Identify the blood parasite species.
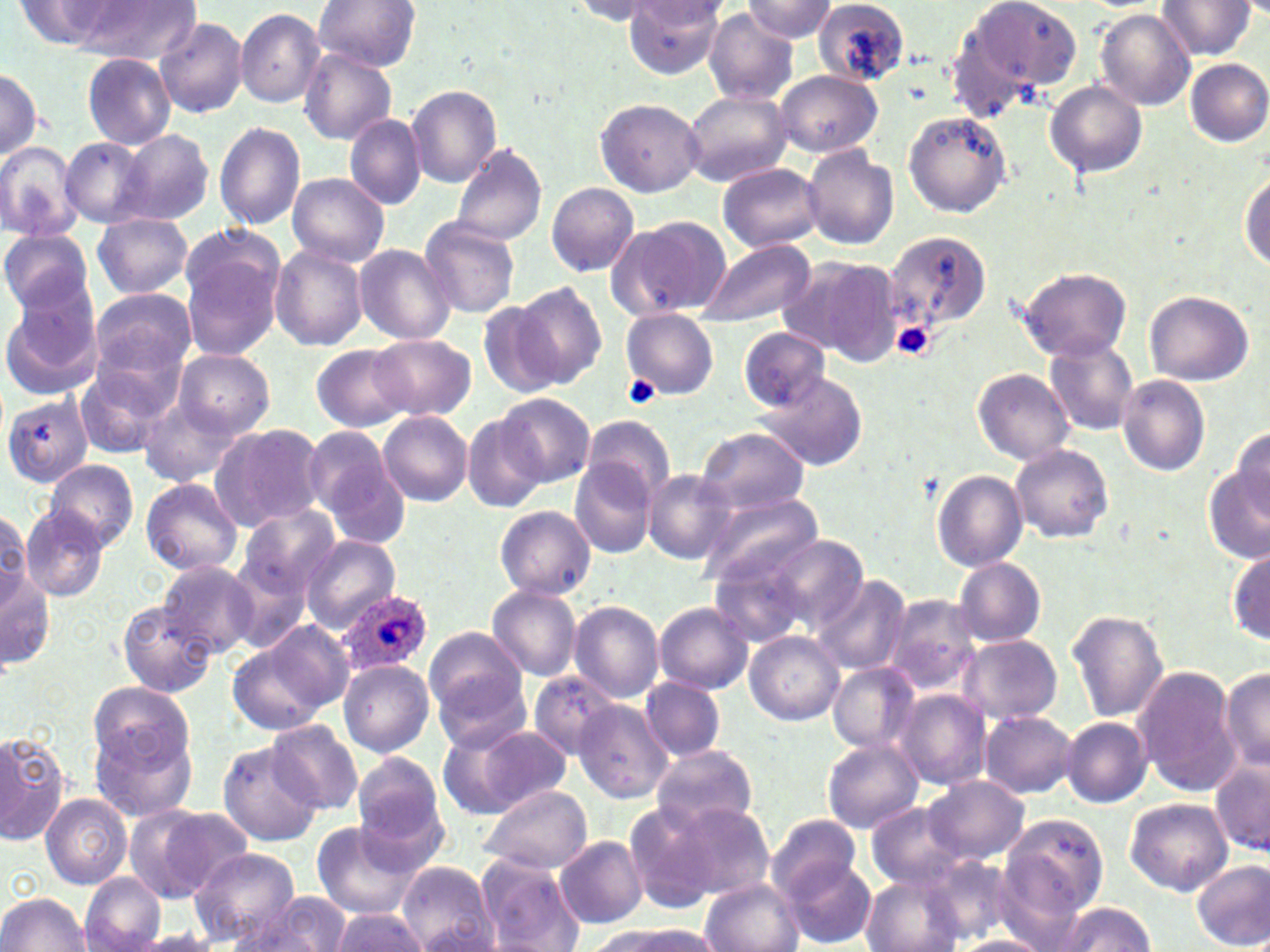
Plasmodium ovale.

Approximate bounding boxes as [x1, y1, x2, y2] in pixels. Platelet locations: [893, 321, 936, 361], [623, 374, 661, 409]. Uninfected red blood cell locations: [314, 0, 422, 72], [624, 0, 726, 78], [745, 0, 837, 42], [953, 0, 1082, 109], [813, 1, 910, 86], [1157, 1, 1258, 59], [12, 2, 143, 51], [61, 2, 201, 61], [570, 2, 674, 27], [234, 8, 325, 107], [1094, 8, 1196, 110], [705, 10, 798, 105], [155, 16, 248, 118], [299, 48, 396, 144], [82, 52, 178, 151], [1185, 58, 1270, 147], [0, 68, 43, 161], [773, 70, 882, 158], [1045, 80, 1148, 179], [406, 86, 502, 186], [683, 90, 793, 188], [595, 97, 705, 196], [902, 110, 1013, 217], [344, 114, 428, 211], [214, 121, 307, 232], [117, 129, 215, 227], [60, 135, 152, 226], [0, 141, 84, 242], [450, 143, 548, 248], [802, 145, 899, 249], [429, 159, 534, 296], [718, 164, 824, 252], [287, 174, 389, 267], [1241, 174, 1269, 271], [546, 181, 640, 277], [92, 214, 193, 298], [607, 215, 731, 320], [420, 216, 521, 319], [184, 221, 279, 305], [0, 228, 94, 318], [884, 230, 992, 336], [696, 240, 815, 329], [181, 244, 284, 359], [269, 244, 368, 351], [354, 244, 458, 344], [780, 255, 903, 366], [1015, 265, 1133, 362], [511, 281, 607, 388], [1, 286, 102, 396], [86, 286, 197, 391], [1144, 290, 1255, 386], [477, 298, 566, 399], [622, 308, 719, 399], [739, 327, 831, 411], [370, 335, 475, 420], [1044, 337, 1141, 436], [310, 345, 413, 432], [173, 348, 275, 437], [74, 361, 177, 457], [972, 368, 1076, 466], [754, 374, 869, 471], [1117, 375, 1210, 476], [496, 393, 594, 486], [4, 395, 95, 486], [138, 395, 246, 487], [379, 412, 473, 505], [462, 414, 549, 512], [580, 415, 676, 504], [210, 423, 326, 530], [304, 424, 403, 529], [695, 426, 811, 516], [1229, 427, 1269, 515], [1010, 444, 1113, 543], [43, 459, 138, 551], [570, 460, 656, 559], [641, 468, 734, 564], [1206, 469, 1270, 563], [932, 470, 1029, 570], [141, 477, 244, 577], [694, 487, 825, 590], [234, 504, 341, 604], [495, 506, 596, 599], [21, 507, 109, 602], [0, 512, 37, 608], [300, 535, 399, 630], [770, 535, 867, 632], [225, 539, 322, 652], [709, 545, 819, 650], [1229, 548, 1269, 645], [954, 558, 1046, 646], [1, 560, 54, 672], [157, 561, 261, 656], [811, 575, 912, 677], [487, 585, 582, 681], [885, 594, 980, 694], [115, 600, 217, 697], [569, 601, 664, 703], [654, 601, 753, 694], [1068, 610, 1168, 722], [227, 622, 354, 735], [424, 629, 529, 723], [745, 631, 843, 725], [957, 635, 1063, 724], [339, 660, 434, 757], [432, 661, 533, 756], [828, 664, 920, 753], [1134, 665, 1241, 795], [1220, 669, 1270, 771], [529, 671, 622, 760], [640, 677, 726, 760], [89, 680, 192, 776], [896, 690, 991, 791], [574, 701, 674, 803], [981, 710, 1079, 797], [89, 713, 199, 826], [1062, 716, 1152, 807], [265, 720, 365, 816], [439, 722, 574, 820], [0, 731, 67, 846], [821, 740, 924, 833], [216, 741, 321, 846], [650, 744, 759, 838], [352, 754, 448, 861], [1211, 756, 1269, 857], [922, 775, 1029, 865], [479, 784, 592, 874], [41, 793, 131, 889], [1126, 797, 1232, 895], [622, 799, 732, 914], [670, 801, 774, 899], [124, 803, 250, 904], [870, 804, 973, 888], [1001, 814, 1109, 923], [768, 816, 866, 906], [310, 821, 424, 918], [554, 835, 647, 928], [189, 847, 302, 947], [474, 855, 583, 952], [782, 858, 877, 947], [1191, 860, 1269, 950], [397, 862, 497, 951], [861, 873, 961, 951], [80, 874, 167, 952], [700, 878, 802, 952], [1, 893, 92, 951], [243, 893, 353, 952], [1052, 901, 1156, 952], [330, 907, 428, 951], [586, 923, 717, 952], [127, 931, 226, 952], [954, 935, 1050, 952]. Plasmodium ovale-infected red blood cell locations: [337, 588, 433, 675]. May-Grünwald-Giemsa stain. Thin blood smear. Light microscopy. Single field of view. Image is 1270×952 pixels. 1000x magnification.